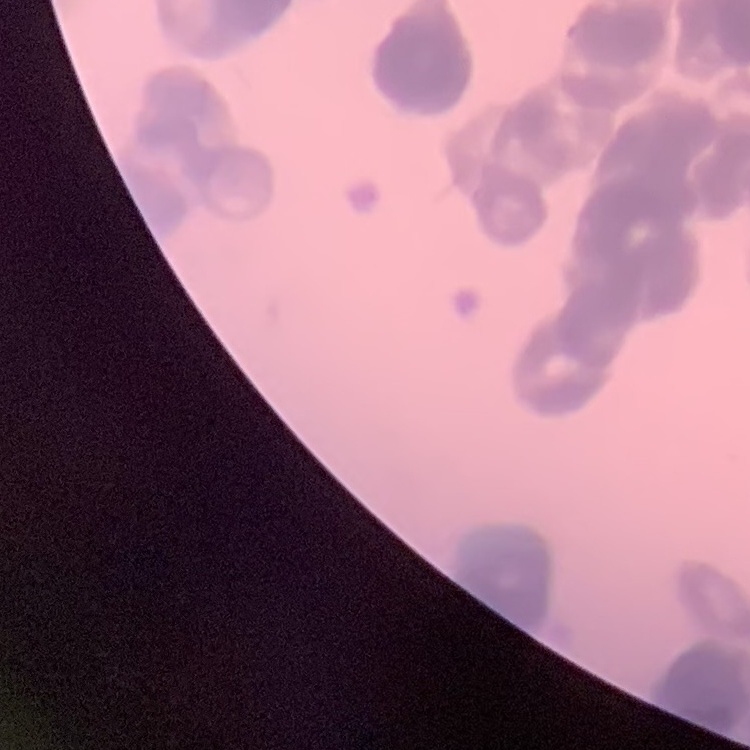
Summary:
  - Erythrocyte morphology: rouleaux formation
  - Preparation: thin blood film
  - Stain: Field's or Giemsa
  - Image type: one tile cut from a larger photomicrograph